Report the malaria status of this cell.
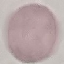
It is uninfected.

{
  "image_type": "cell patch, automatically extracted from a larger field of view and resized to 64 × 64 pixels",
  "preparation": "thin smear",
  "stain": "Giemsa",
  "capture": "smartphone through the microscope eyepiece"
}